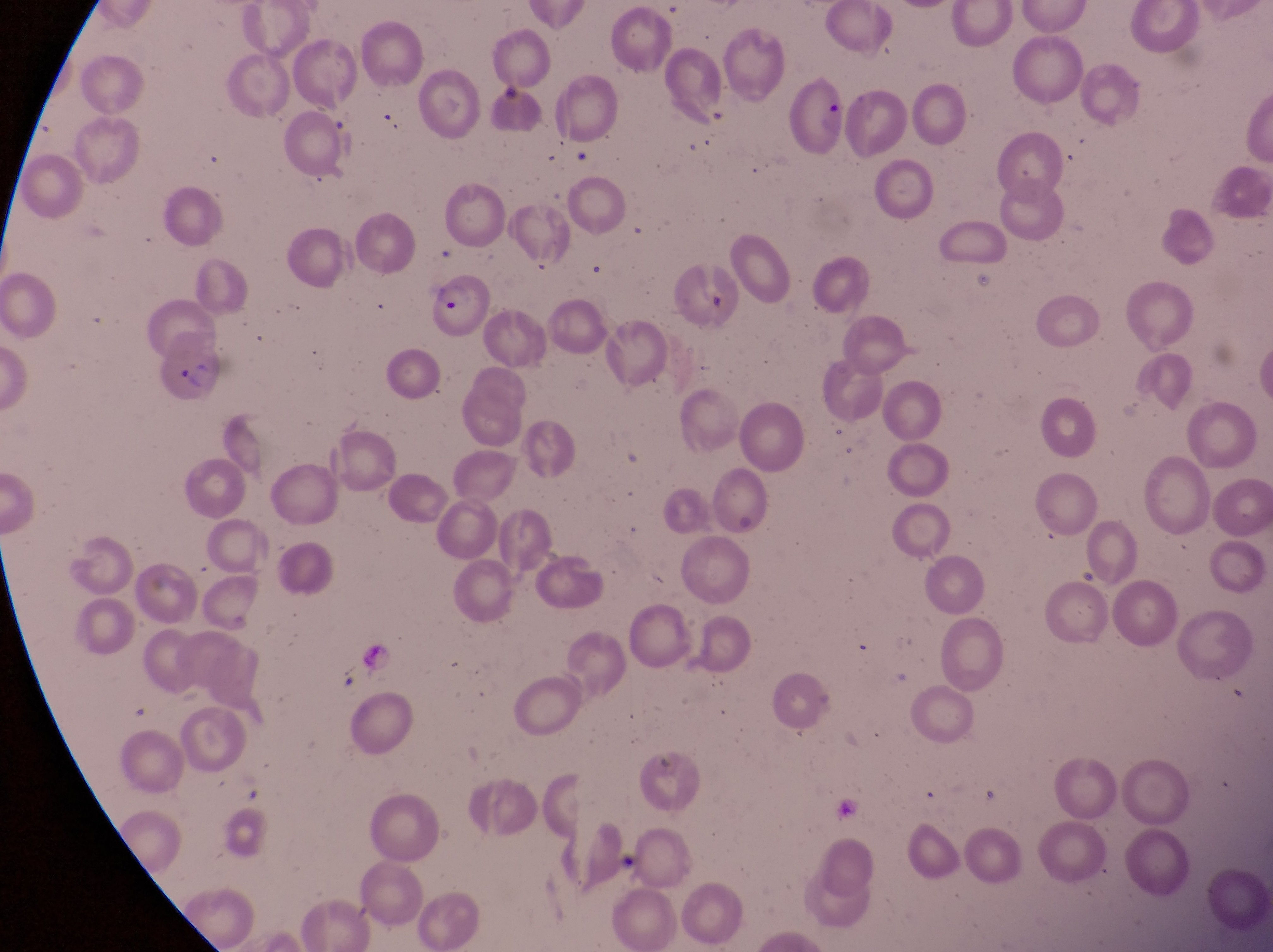
country = Uganda
preparation = thin blood film
image size = 1273×952 pixels
parasitised red blood cell locations = approximate bounding boxes as {left, top, right, bottom} in pixels: {434, 270, 491, 342}, {150, 335, 224, 407}
field of view = single
magnification = 1000x
capture = smartphone photograph through the eyepiece of an Olympus CX-23 microscope